Comment on the morphology of the erythrocytes.
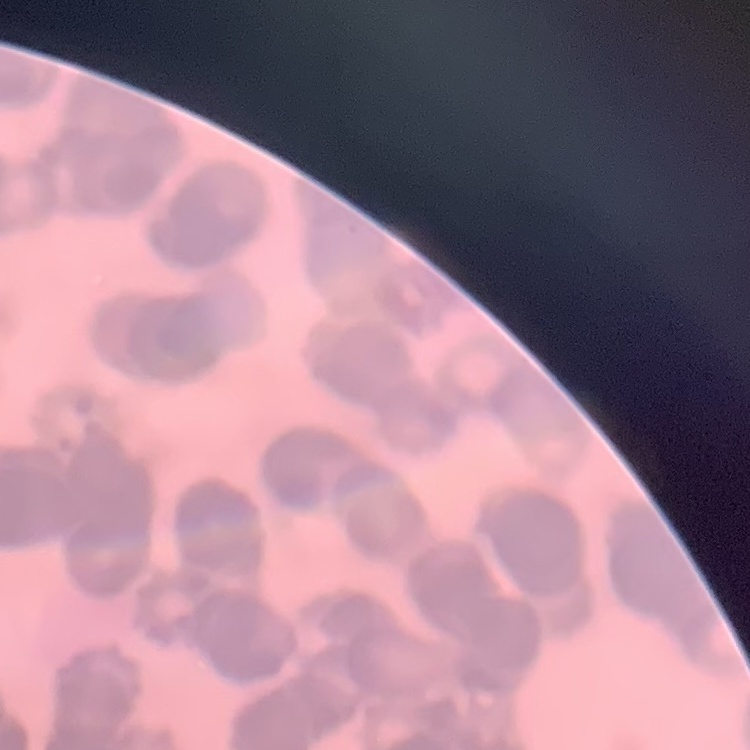
They show rouleaux formation.

stain = Field's or Giemsa
image type = square crop of a larger photomicrograph
preparation = thin blood smear